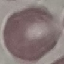
result = negative for malaria parasites
image type = cell patch, automatically extracted from a larger field of view and resized to 64 × 64 pixels
stain = Giemsa
capture = smartphone camera at the microscope eyepiece
preparation = thin blood smear